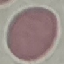
Summary:
  - Result: negative for malaria parasites
  - Image type: automatically extracted cell patch, resized to 64 × 64 pixels
  - Preparation: thin blood smear
  - Stain: Giemsa
  - Capture: smartphone camera at the microscope eyepiece